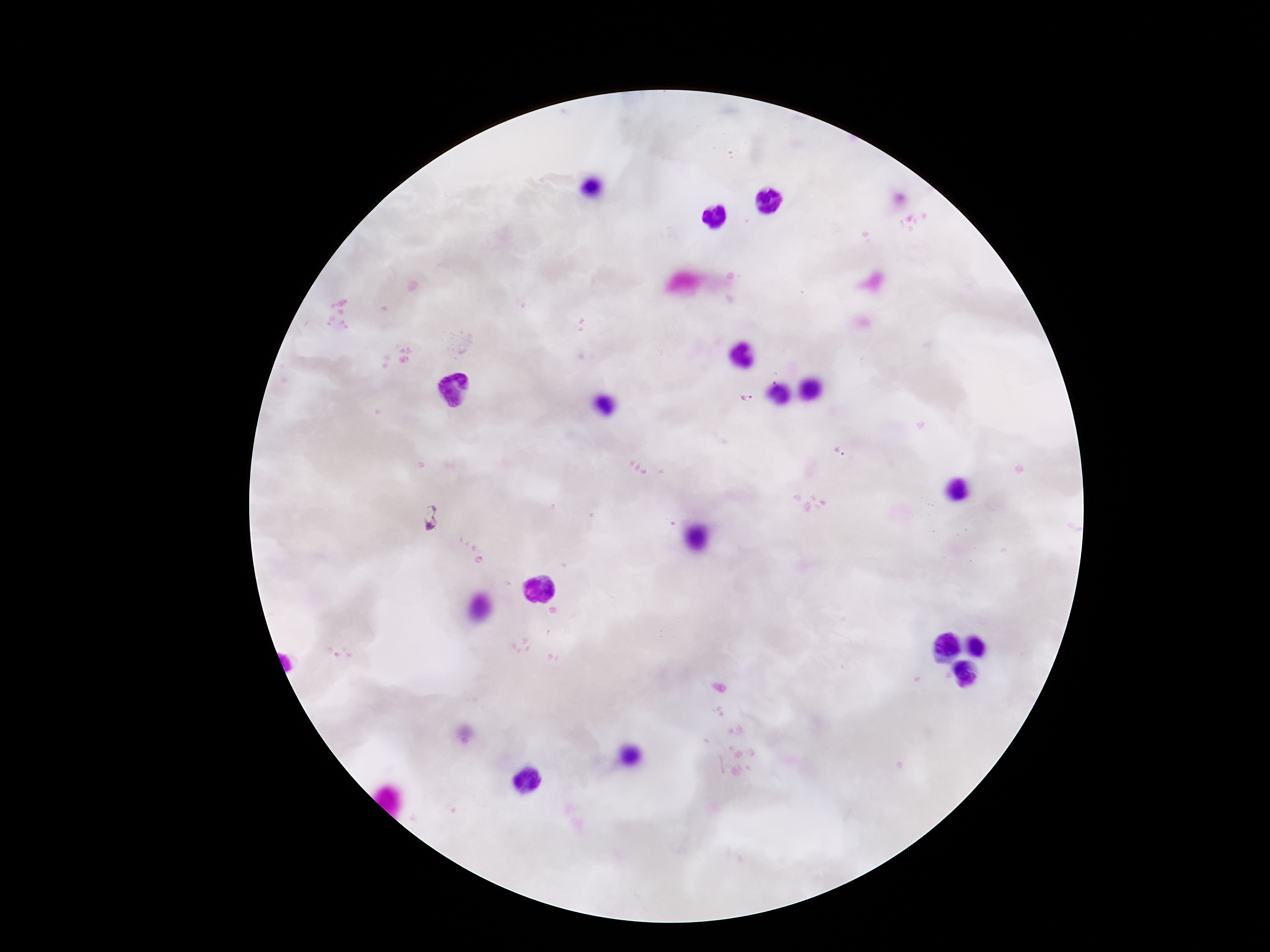 Approximate centers as {x, y} in pixels. Plasmodium parasite locations: {747, 397}, {841, 452}, {433, 518}. Image is 1270×952 pixels. One field from this slide. Photographed through the microscope eyepiece with a smartphone camera. Patient malaria status: infected. Giemsa-stained preparation. Thick blood smear. 100x magnification.